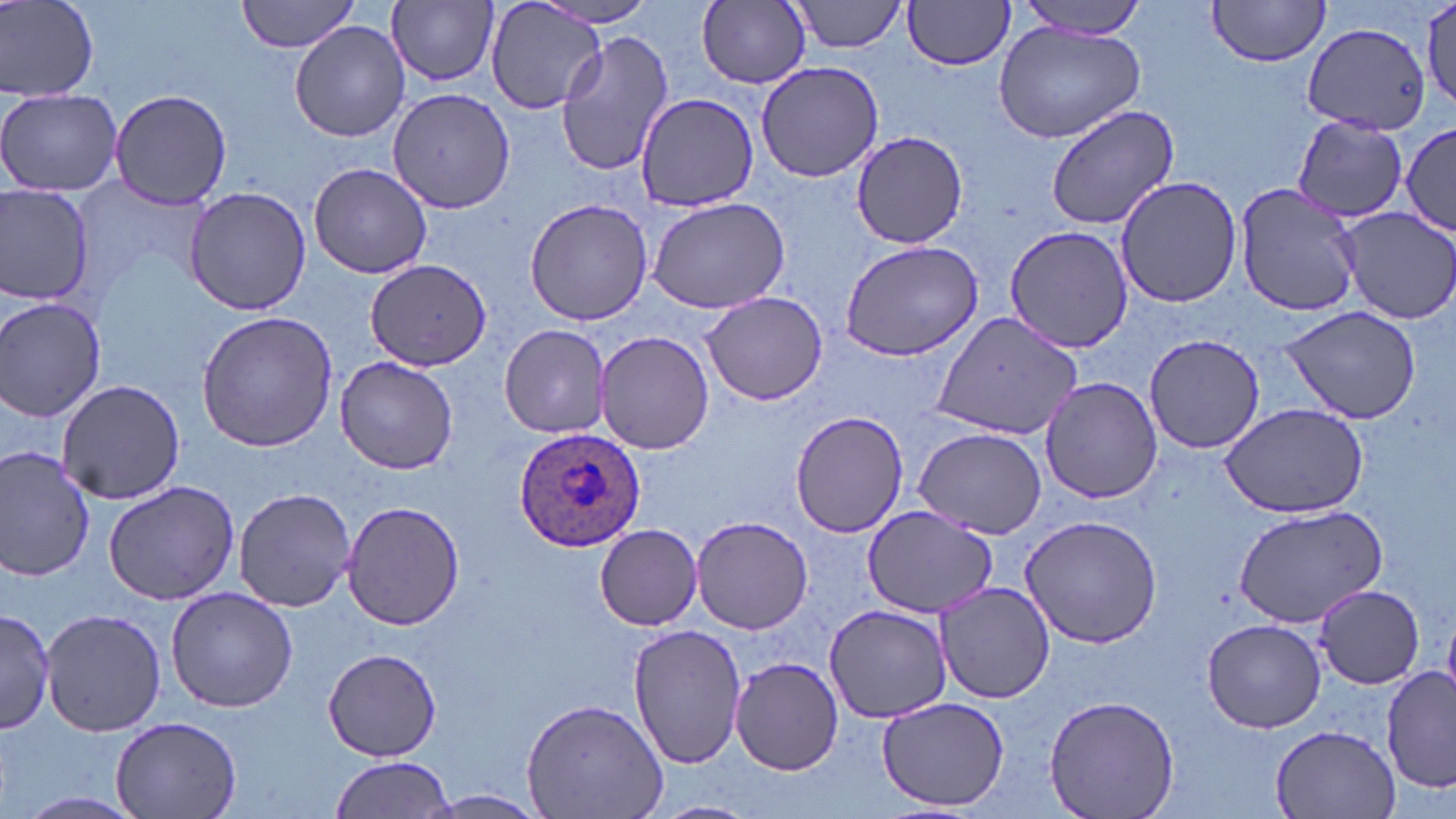
Summary:
  - Coordinate format: approximate bounding boxes as (x1, y1, x2, y2) in pixels
  - Uninfected red blood cell locations: (2, 0, 99, 100), (235, 0, 366, 54), (484, 0, 607, 116), (788, 0, 909, 54), (903, 0, 1017, 71), (1014, 0, 1153, 40), (1206, 0, 1332, 67), (388, 1, 498, 87), (535, 1, 664, 29), (1420, 1, 1456, 111), (697, 2, 810, 89), (290, 21, 409, 143), (994, 21, 1145, 142), (1305, 21, 1433, 132), (554, 29, 674, 179), (757, 60, 884, 184), (0, 87, 122, 197), (108, 88, 232, 208), (387, 88, 516, 213), (633, 93, 760, 210), (1045, 103, 1178, 231), (1292, 115, 1411, 223), (1401, 120, 1454, 241), (848, 130, 969, 248), (308, 162, 434, 279), (1115, 175, 1243, 308), (1235, 181, 1363, 319), (0, 183, 95, 309), (184, 185, 311, 316), (646, 195, 791, 314), (524, 198, 654, 327), (1337, 207, 1456, 324), (1002, 224, 1136, 354), (839, 238, 986, 361), (364, 257, 491, 369), (700, 290, 831, 406), (0, 297, 107, 423), (1279, 305, 1422, 425), (196, 309, 337, 453), (929, 310, 1083, 441), (499, 324, 614, 438), (596, 331, 714, 455), (1142, 334, 1268, 455), (336, 355, 458, 476), (1040, 377, 1165, 503), (57, 379, 187, 503), (1219, 402, 1370, 519), (789, 409, 910, 537), (911, 426, 1048, 536), (0, 446, 96, 583), (103, 480, 243, 606), (232, 486, 359, 612), (341, 500, 467, 631), (1233, 505, 1389, 628), (862, 507, 996, 619), (1016, 514, 1163, 649), (691, 515, 813, 635), (594, 524, 702, 630), (934, 579, 1056, 703), (1317, 584, 1426, 690), (166, 587, 298, 714), (824, 606, 952, 721), (41, 607, 165, 736), (0, 610, 58, 734), (1203, 618, 1326, 733), (628, 625, 747, 770), (323, 649, 442, 760), (730, 656, 843, 776), (1382, 667, 1455, 794), (1044, 694, 1179, 819), (876, 696, 1010, 812), (520, 697, 669, 819), (111, 714, 241, 819), (1268, 723, 1404, 817), (328, 754, 456, 819), (422, 790, 546, 816), (18, 791, 144, 816), (647, 800, 760, 819)
  - Plasmodium ovale-infected red blood cell locations: (513, 426, 645, 554)
  - Slide-level diagnosis: Plasmodium ovale
  - Preparation: thin blood film
  - Modality: light microscopy
  - Image size: 1456×819 pixels
  - Field of view: one of a larger specimen
  - Stain: May-Grünwald-Giemsa
  - Magnification: 1000x